Identify the parasite.
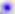

This is Toxoplasma gondii.

Summary:
  - Modality: micrograph
  - Magnification: 400x